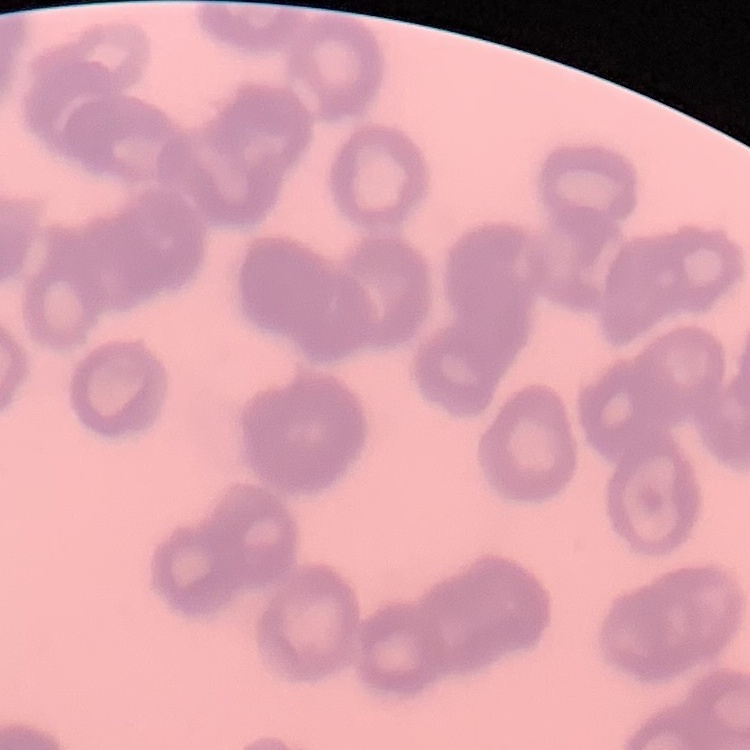

The red blood cells exhibit rouleaux formation. Square crop of a larger photomicrograph. Thin blood smear. Field's or Giemsa stain.